State which cell type is depicted.
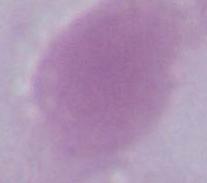

This is an erythrocyte.

{
  "modality": "photomicrograph",
  "magnification": "1000x"
}